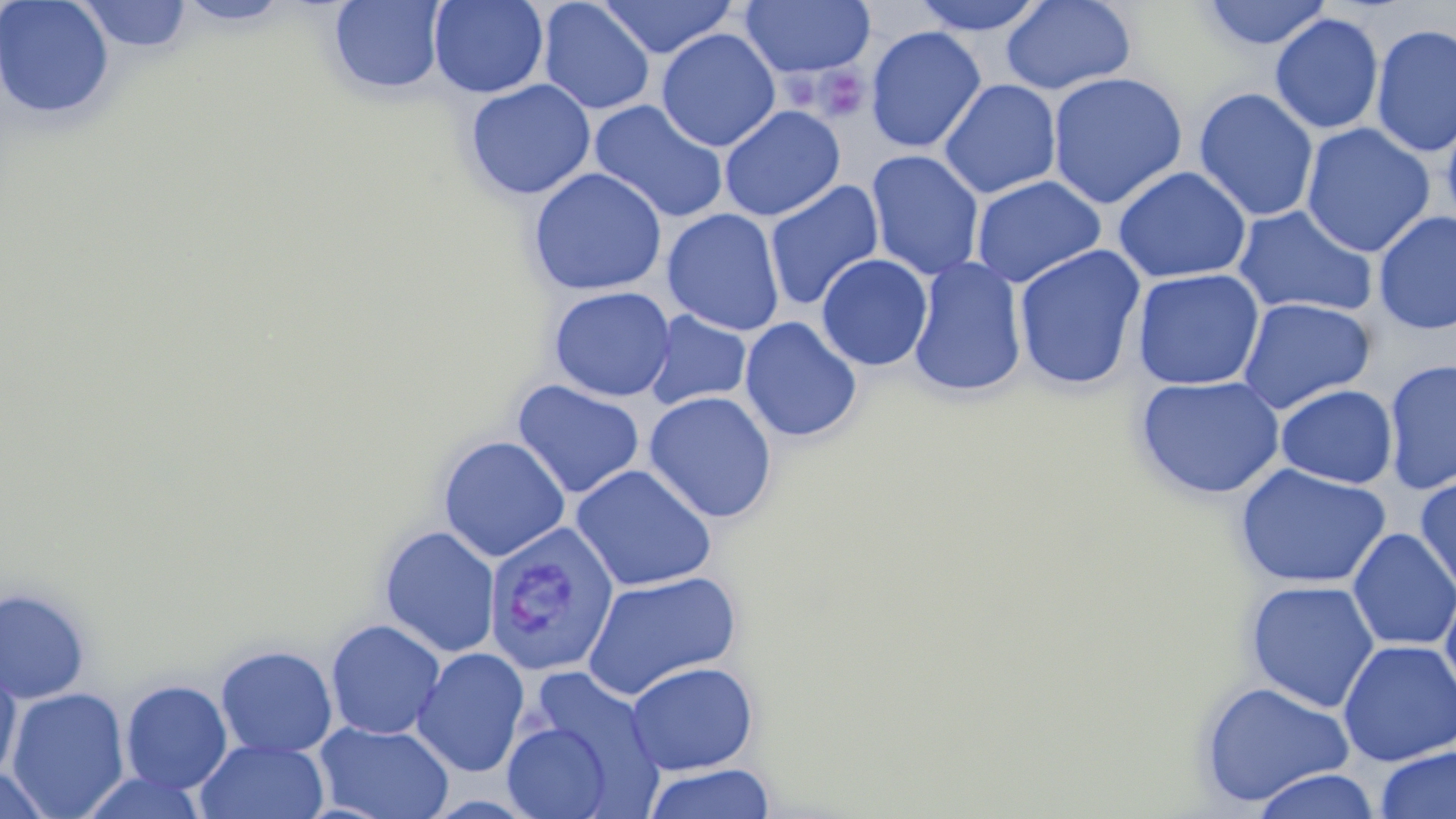
slide-level diagnosis = Plasmodium vivax
platelet locations = approximate bounding boxes as named x1/y1/x2/y2 corners in pixels: (x1=813, y1=66, x2=870, y2=123)
preparation = thin blood film
modality = light microscopy
field of view = single
magnification = 1000x
Plasmodium vivax-infected red blood cell locations = approximate bounding boxes as named x1/y1/x2/y2 corners in pixels: (x1=483, y1=523, x2=620, y2=678)
stain = May-Grünwald-Giemsa
uninfected red blood cell locations = approximate bounding boxes as named x1/y1/x2/y2 corners in pixels: (x1=0, y1=0, x2=116, y2=121), (x1=76, y1=0, x2=193, y2=54), (x1=175, y1=0, x2=293, y2=28), (x1=428, y1=0, x2=549, y2=98), (x1=597, y1=0, x2=738, y2=59), (x1=909, y1=0, x2=1049, y2=36), (x1=1000, y1=0, x2=1137, y2=95), (x1=1200, y1=0, x2=1333, y2=50), (x1=328, y1=1, x2=448, y2=96), (x1=537, y1=1, x2=655, y2=115), (x1=740, y1=1, x2=876, y2=79), (x1=1269, y1=13, x2=1384, y2=134), (x1=1370, y1=23, x2=1456, y2=158), (x1=865, y1=25, x2=986, y2=154), (x1=656, y1=28, x2=781, y2=152), (x1=1047, y1=72, x2=1188, y2=209), (x1=464, y1=79, x2=596, y2=200), (x1=939, y1=79, x2=1061, y2=199), (x1=1193, y1=87, x2=1320, y2=222), (x1=588, y1=99, x2=730, y2=224), (x1=719, y1=105, x2=846, y2=222), (x1=1441, y1=108, x2=1456, y2=232), (x1=1300, y1=123, x2=1435, y2=258), (x1=866, y1=150, x2=985, y2=280), (x1=1112, y1=166, x2=1252, y2=284), (x1=528, y1=167, x2=667, y2=296), (x1=971, y1=175, x2=1106, y2=288), (x1=763, y1=180, x2=884, y2=312), (x1=1233, y1=205, x2=1378, y2=319), (x1=662, y1=208, x2=785, y2=336), (x1=1373, y1=210, x2=1456, y2=335), (x1=1013, y1=244, x2=1146, y2=391), (x1=816, y1=253, x2=933, y2=371), (x1=908, y1=256, x2=1027, y2=398), (x1=1131, y1=268, x2=1265, y2=390), (x1=548, y1=286, x2=676, y2=402), (x1=1237, y1=297, x2=1375, y2=414), (x1=644, y1=310, x2=752, y2=411), (x1=739, y1=316, x2=862, y2=443), (x1=1383, y1=359, x2=1456, y2=495), (x1=1134, y1=374, x2=1285, y2=500), (x1=512, y1=379, x2=646, y2=499), (x1=1274, y1=384, x2=1398, y2=489), (x1=643, y1=391, x2=778, y2=524), (x1=438, y1=435, x2=571, y2=562), (x1=1233, y1=463, x2=1392, y2=589), (x1=571, y1=464, x2=717, y2=592), (x1=1414, y1=476, x2=1456, y2=598), (x1=379, y1=525, x2=501, y2=657), (x1=1348, y1=528, x2=1456, y2=652), (x1=581, y1=570, x2=742, y2=701), (x1=1244, y1=578, x2=1380, y2=713), (x1=1439, y1=580, x2=1456, y2=707), (x1=0, y1=587, x2=91, y2=704), (x1=325, y1=619, x2=446, y2=740), (x1=1338, y1=639, x2=1456, y2=766), (x1=215, y1=645, x2=337, y2=758), (x1=411, y1=647, x2=530, y2=778), (x1=625, y1=660, x2=759, y2=775), (x1=516, y1=667, x2=666, y2=812), (x1=0, y1=673, x2=22, y2=780), (x1=120, y1=680, x2=233, y2=794), (x1=1198, y1=680, x2=1356, y2=808), (x1=6, y1=687, x2=130, y2=818), (x1=502, y1=719, x2=614, y2=819), (x1=314, y1=721, x2=454, y2=819), (x1=196, y1=739, x2=329, y2=819), (x1=1375, y1=746, x2=1456, y2=819), (x1=642, y1=762, x2=777, y2=819), (x1=0, y1=764, x2=55, y2=819), (x1=1250, y1=768, x2=1382, y2=819)
image size = 1456×819 pixels